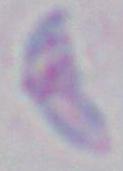
identification = Toxoplasma gondii
modality = photomicrograph
magnification = 1000x